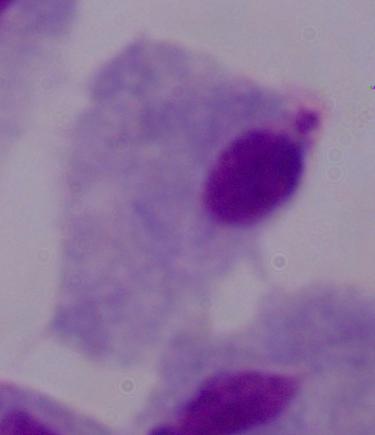 1000x magnification. A trichomonad is shown. Micrograph.